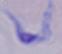

Captured at 1000x magnification. Photomicrograph. A trypanosome is shown.